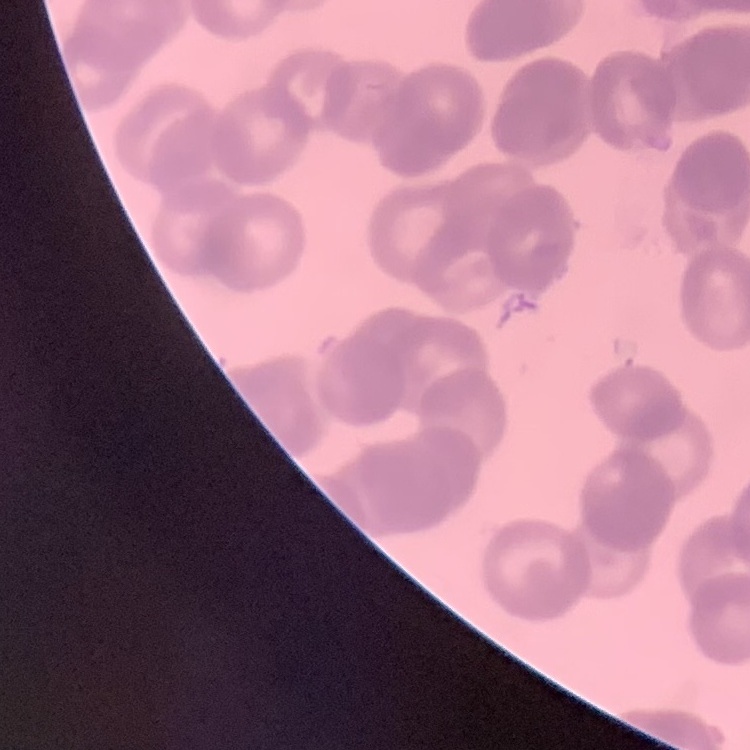

Summary:
  - Red blood cell morphology: rouleaux formation
  - Preparation: thin blood smear
  - Image type: one tile cut from a larger photomicrograph
  - Stain: Field's or Giemsa